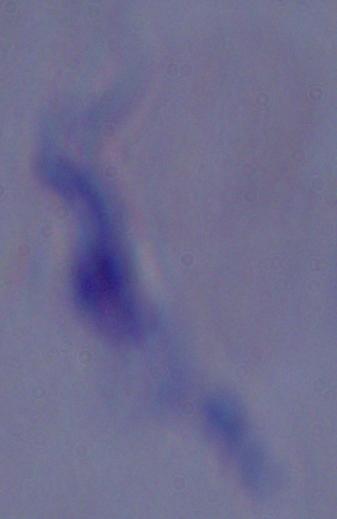
Photomicrograph. Captured at 1000x magnification. A trypanosome is seen.